Describe the morphology of the red blood cells.
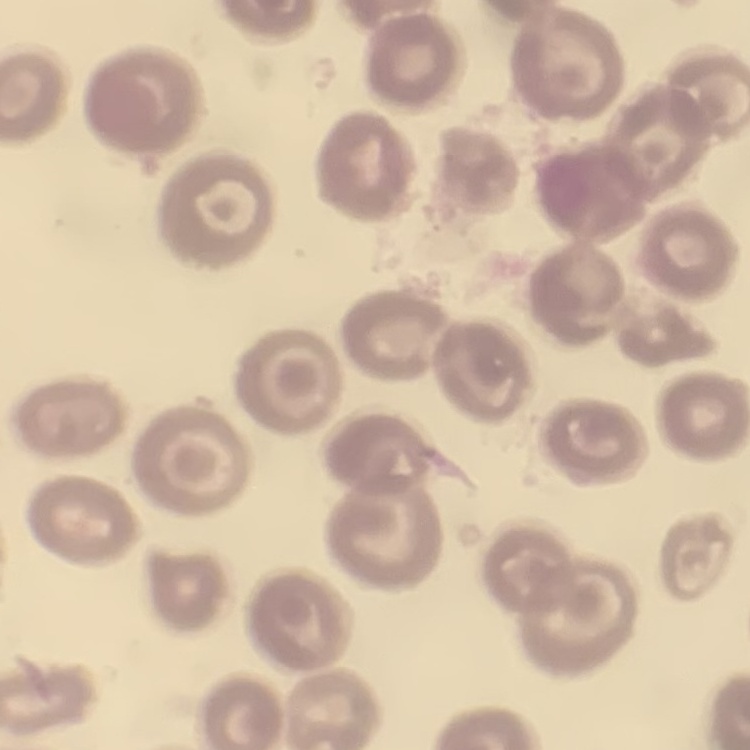

No rouleaux formation.

Summary:
  - Image type: square crop of a larger photomicrograph
  - Stain: Field's or Giemsa
  - Preparation: thin blood film